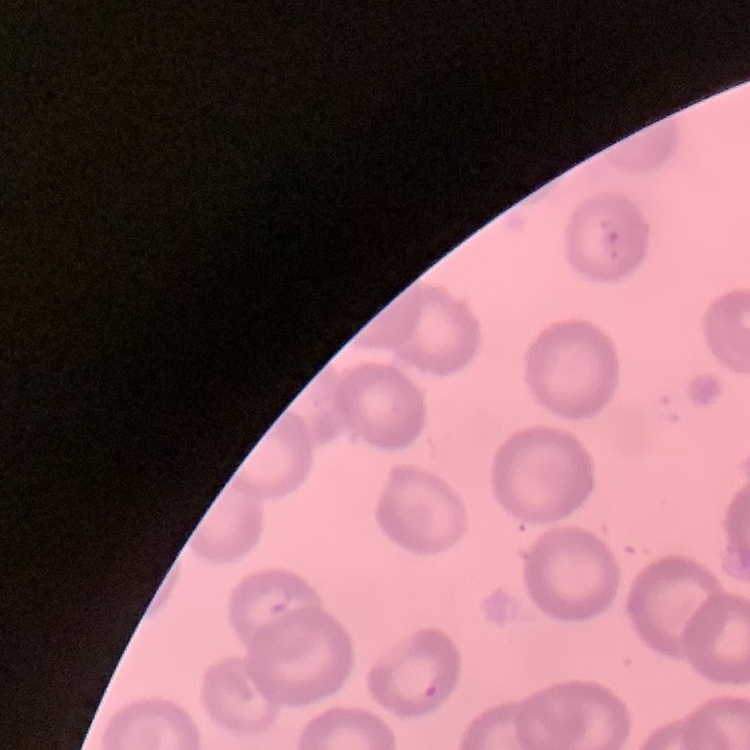

Summary:
  - Red blood cell morphology: no rouleaux formation
  - Preparation: thin peripheral smear
  - Image type: square crop of a larger photomicrograph
  - Stain: Field's or Giemsa